Outline each white blood cell.
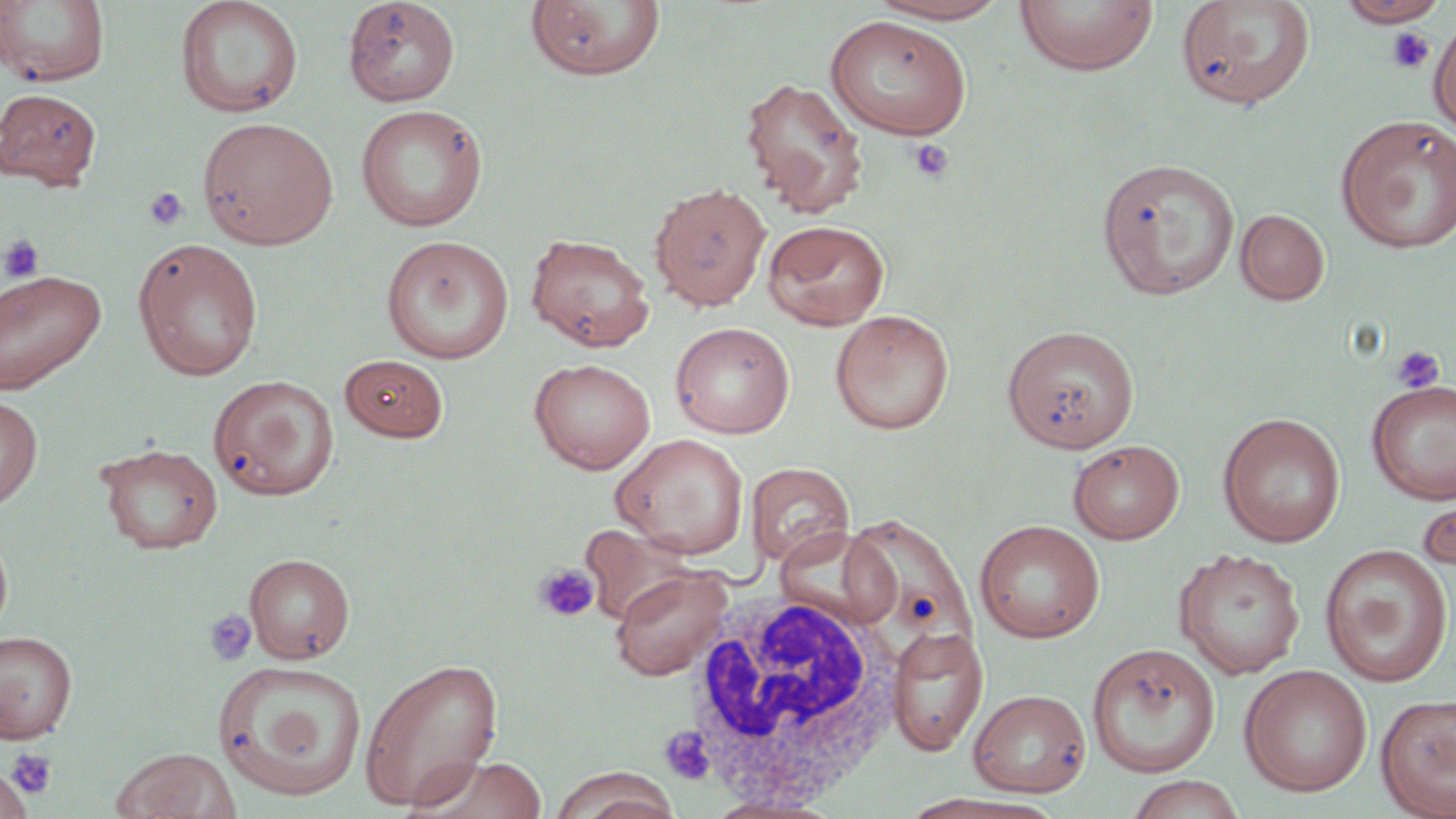

Approximate bounding boxes as [x1, y1, x2, y2] in pixels.
White blood cells: [674, 589, 908, 807].

Platelet locations: [1386, 28, 1435, 75], [908, 138, 953, 183], [144, 186, 189, 231], [2, 235, 46, 283], [1390, 346, 1445, 393], [534, 562, 600, 623], [203, 610, 258, 666], [659, 727, 716, 785], [5, 748, 58, 800]. Uninfected red blood cell locations: [175, 0, 303, 118], [342, 0, 461, 107], [865, 0, 1014, 24], [1014, 0, 1159, 77], [1175, 0, 1316, 111], [0, 1, 109, 89], [525, 1, 667, 81], [1335, 1, 1450, 27], [825, 15, 972, 140], [1428, 16, 1456, 138], [739, 75, 869, 217], [0, 87, 101, 189], [355, 104, 488, 232], [1336, 115, 1456, 254], [197, 117, 339, 249], [1097, 158, 1240, 299], [648, 182, 771, 311], [1235, 208, 1330, 305], [762, 220, 890, 330], [526, 233, 655, 352], [381, 235, 515, 363], [132, 237, 264, 381], [0, 269, 106, 395], [525, 280, 669, 438], [829, 310, 955, 434], [670, 321, 795, 439], [1002, 324, 1140, 452], [340, 354, 450, 442], [529, 357, 656, 474], [209, 375, 338, 500], [1366, 378, 1456, 505], [0, 393, 43, 510], [1217, 411, 1345, 548], [611, 433, 750, 558], [1067, 439, 1184, 544], [95, 442, 224, 554], [745, 462, 855, 567], [1416, 480, 1455, 580], [842, 513, 975, 650], [974, 518, 1105, 643], [772, 526, 900, 628], [0, 528, 13, 641], [1319, 543, 1454, 687], [1173, 547, 1305, 679], [244, 552, 356, 663], [609, 565, 733, 681], [887, 627, 988, 756], [0, 631, 78, 744], [1086, 643, 1221, 778], [358, 656, 504, 812], [214, 660, 367, 800], [1238, 664, 1373, 798], [968, 688, 1092, 797], [1375, 693, 1456, 818], [110, 747, 241, 819], [407, 754, 550, 819], [0, 765, 32, 818], [548, 767, 682, 819], [1125, 774, 1247, 818], [900, 793, 1059, 818], [701, 794, 845, 818]. Slide-level diagnosis: negative for blood parasites. Single field of view. Optical microscopy. May-Grünwald-Giemsa stain. Captured at 1000x magnification. Thin blood film. Image is 1456×819 pixels.